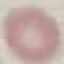
Summary:
  - Result: negative for malaria parasites
  - Image type: cell patch, automatically extracted from a larger field of view and resized to 64 × 64 pixels
  - Capture: smartphone camera at the microscope eyepiece
  - Stain: Giemsa
  - Preparation: thin blood film